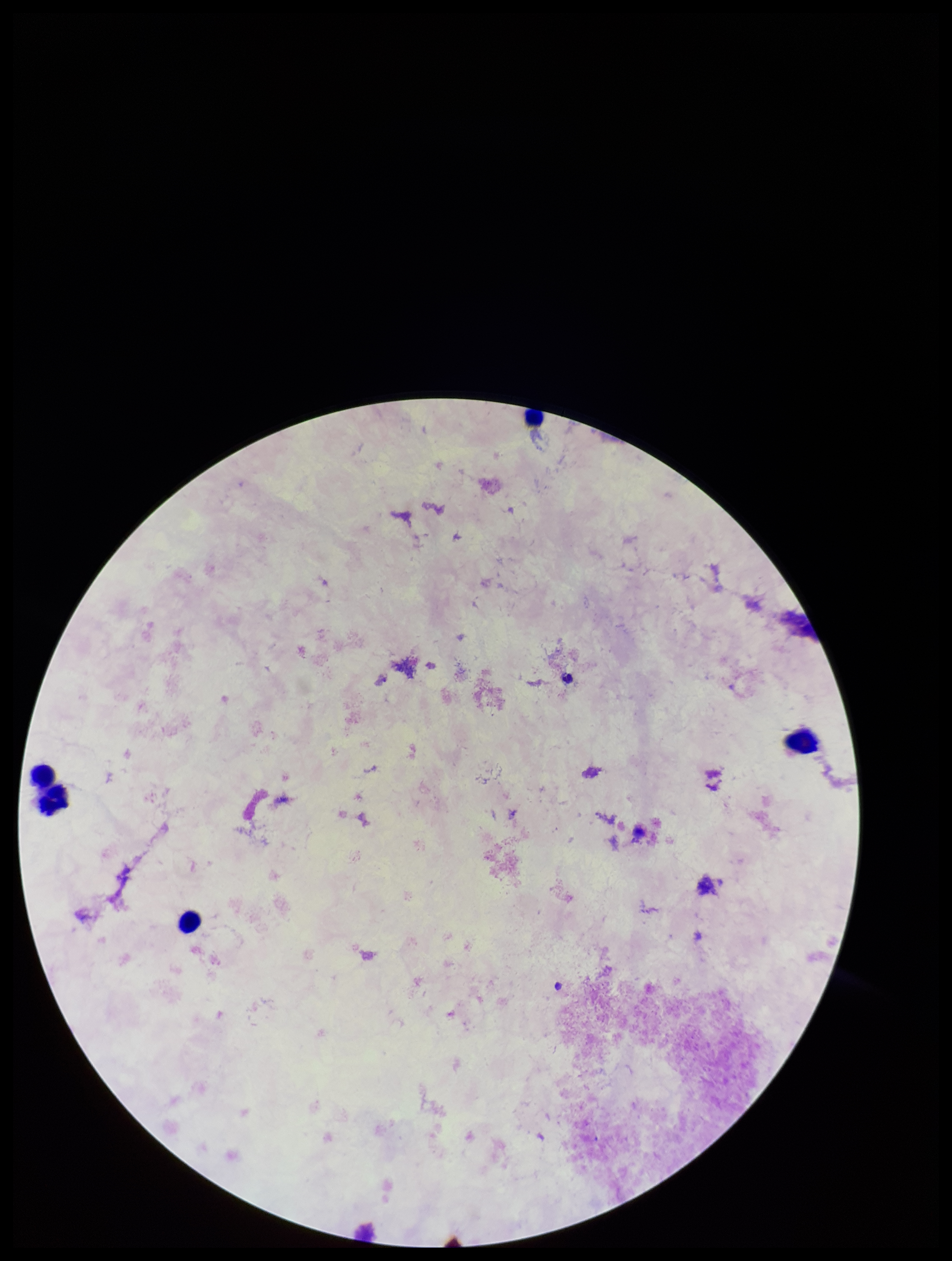

Summary:
  - Capture: smartphone photograph through the microscope eyepiece
  - Preparation: thick blood smear
  - Plasmodium parasites: none seen
  - Leukocyte count: 5
  - Field of view: one from this slide
  - Patient malaria status: negative
  - Stain: Giemsa
  - Parasite count: 0
  - Image size: 952×1261 pixels